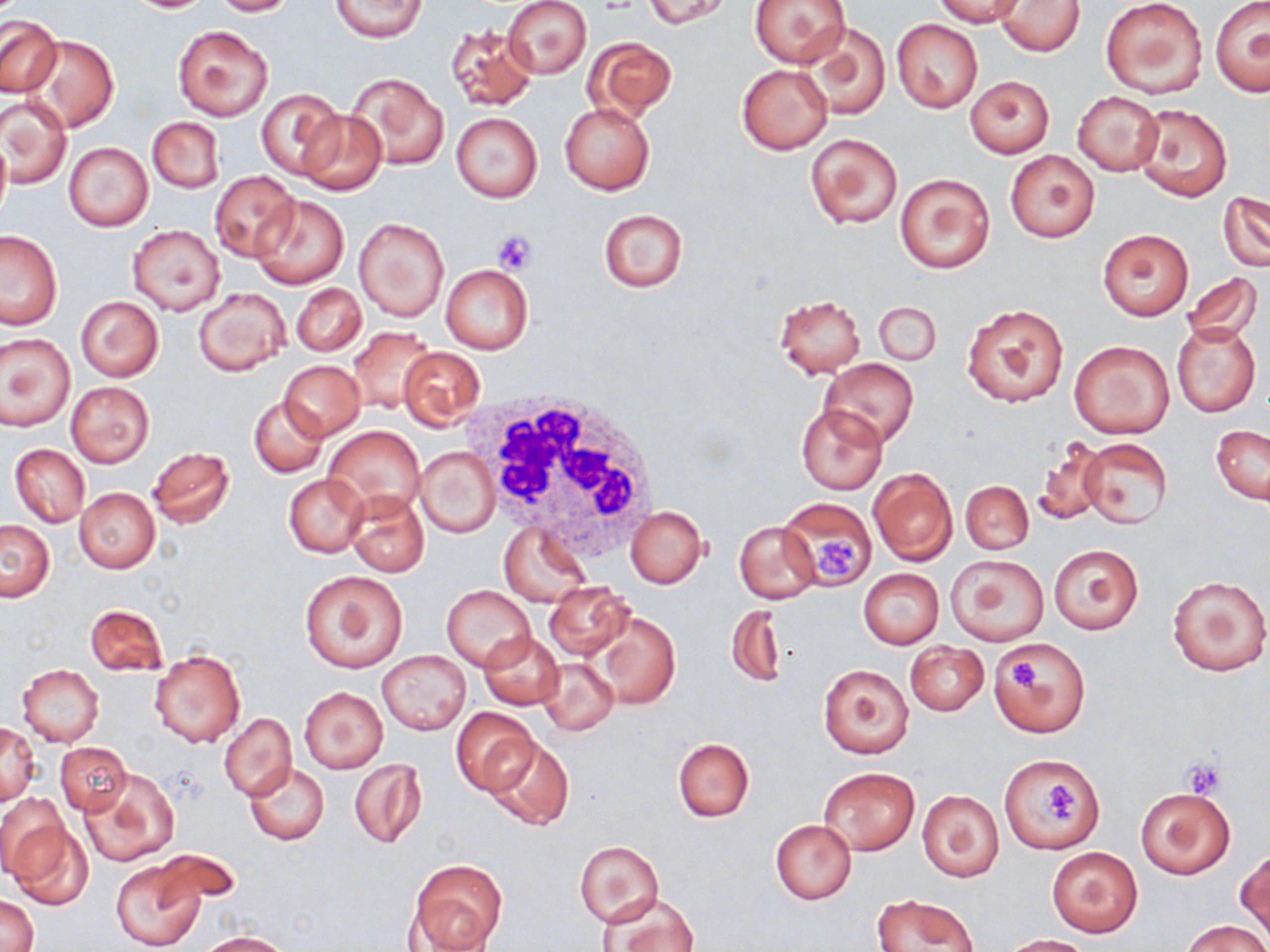
slide_level_diagnosis: no evidence of blood parasites
magnification: 1000x
field_of_view: one of a larger specimen
preparation: thin blood smear
uninfected_red_blood_cell_locations: 'approximate bounding boxes as (x1,y1)-(x2,y2) corner pairs in pixels: (122,0)-(213,13), (209,0)-(296,16), (329,0)-(426,41), (502,0)-(591,79), (643,0)-(732,29), (749,0)-(852,69), (932,0)-(1027,26), (1099,0)-(1208,101), (1210,0)-(1270,98), (996,1)-(1085,55), (1,16)-(62,97), (892,19)-(982,112), (445,23)-(536,111), (803,23)-(890,121), (172,24)-(274,120), (583,34)-(676,122), (24,35)-(117,132), (737,64)-(833,154), (347,71)-(448,171), (965,76)-(1054,157), (257,87)-(345,180), (1072,90)-(1163,177), (2,95)-(71,189), (559,101)-(654,195), (1132,103)-(1232,201), (297,111)-(384,195), (451,113)-(542,202), (147,117)-(225,193), (804,131)-(904,230), (0,132)-(11,224), (63,143)-(153,231), (1005,150)-(1100,243), (209,170)-(300,262), (895,173)-(995,276), (1219,191)-(1270,270), (251,195)-(347,289), (598,208)-(688,293), (354,217)-(448,322), (127,225)-(224,316), (1098,229)-(1193,320), (0,230)-(62,329), (440,264)-(532,354), (1182,271)-(1264,346), (291,284)-(364,356), (194,289)-(290,376), (774,295)-(865,377), (76,296)-(163,382), (872,300)-(940,367), (961,301)-(1070,408), (1170,321)-(1261,417), (349,327)-(437,414), (1,334)-(74,431), (1068,339)-(1174,439), (398,347)-(486,428), (820,358)-(918,449), (279,361)-(364,440), (66,382)-(154,467), (250,398)-(327,478), (796,404)-(886,494), (324,426)-(424,516), (1211,426)-(1269,506), (1031,436)-(1108,526), (1076,438)-(1171,530), (10,444)-(89,527), (148,446)-(235,529), (416,448)-(499,537), (869,468)-(957,567), (284,472)-(369,557), (960,480)-(1033,555), (75,487)-(160,573), (343,489)-(429,577), (780,497)-(877,588), (626,506)-(708,588), (0,521)-(55,601), (735,522)-(820,604), (498,524)-(591,607), (1048,545)-(1143,633), (946,554)-(1049,645), (858,569)-(944,647), (299,570)-(408,673), (1166,573)-(1269,677), (544,581)-(632,659), (442,585)-(535,671), (85,603)-(168,676), (725,603)-(787,689), (592,612)-(680,709), (480,631)-(564,710), (987,638)-(1090,738), (906,642)-(989,716), (377,651)-(469,735), (149,652)-(245,748), (538,658)-(618,737), (16,663)-(104,746), (818,663)-(915,758), (297,687)-(389,773), (452,708)-(539,794), (219,714)-(295,801), (1,724)-(39,806), (483,736)-(575,832), (673,737)-(754,822), (56,742)-(130,816), (1001,755)-(1103,853), (348,759)-(427,851), (244,763)-(328,845), (819,767)-(920,855), (79,769)-(178,866), (1135,786)-(1235,881), (917,789)-(1004,882), (1,792)-(69,881), (8,819)-(91,908), (769,820)-(856,904), (574,841)-(664,927), (1046,847)-(1142,936), (149,849)-(240,909), (1235,849)-(1270,940), (406,860)-(508,952), (112,861)-(204,950), (600,891)-(699,952), (0,894)-(38,952), (872,894)-(979,951), (1183,919)-(1267,952), (196,931)-(293,952), (1001,934)-(1092,951)'
modality: light microscopy
stain: May-Grünwald-Giemsa
white_blood_cell_locations: 'approximate bounding boxes as (x1,y1)-(x2,y2) corner pairs in pixels: (476,388)-(661,558)'
platelet_locations: 'approximate bounding boxes as (x1,y1)-(x2,y2) corner pairs in pixels: (492,229)-(537,274), (813,532)-(859,581), (1010,660)-(1043,695), (1179,759)-(1226,798), (1044,783)-(1075,820)'
image_size: 1270×952 pixels